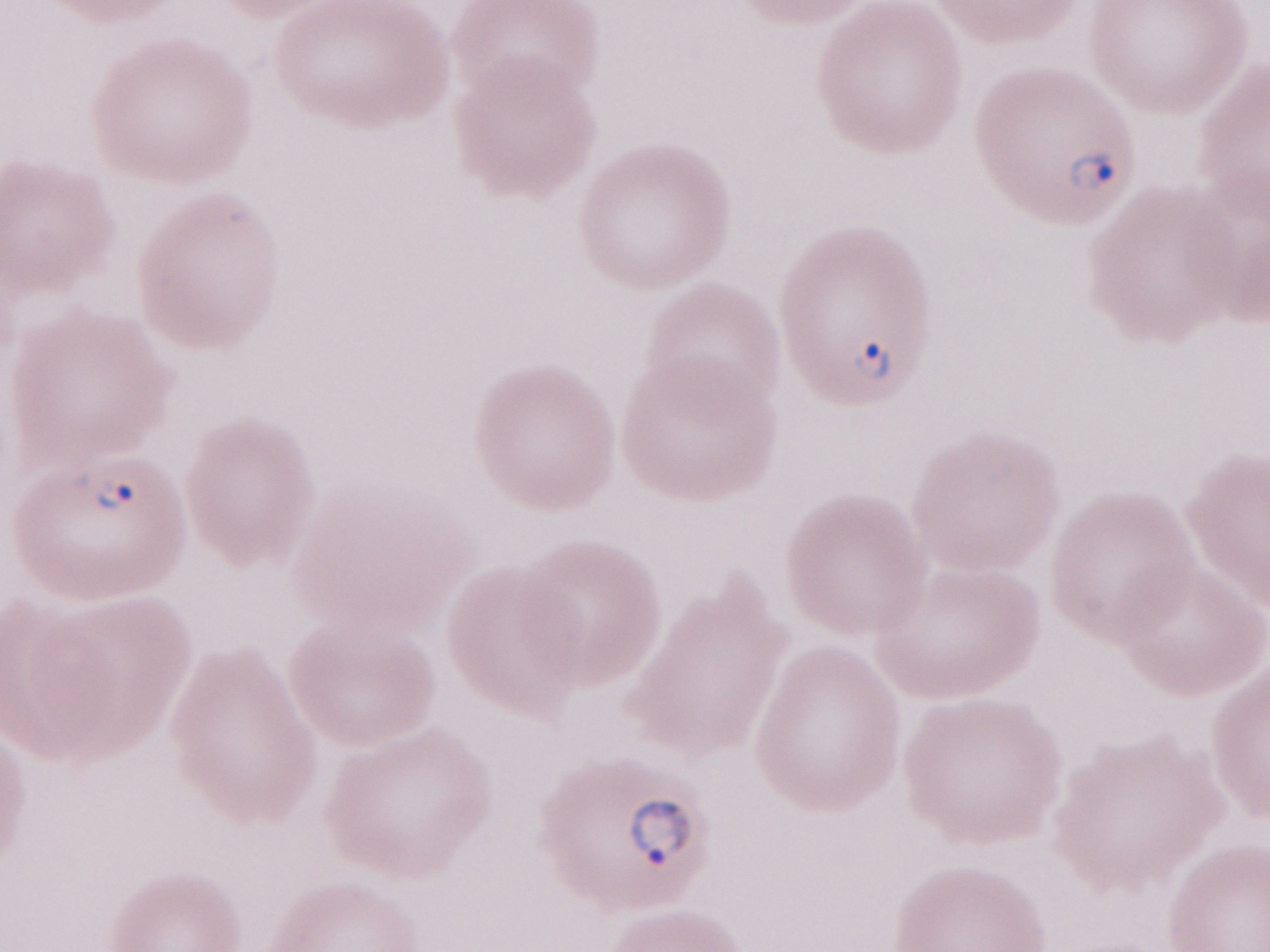

One field of this slide. Patient diagnosis: malaria infection. Thin peripheral-blood smear. Image is 1270×952 pixels. Olympus BX43 microscope and DP73 digital camera. May-Grünwald-Giemsa stain. Magnification: 1,000x.